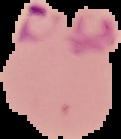

Image is 121×139 pixels. Result: Plasmodium parasites detected. From a thin blood film. Segmented cell region on a black background.